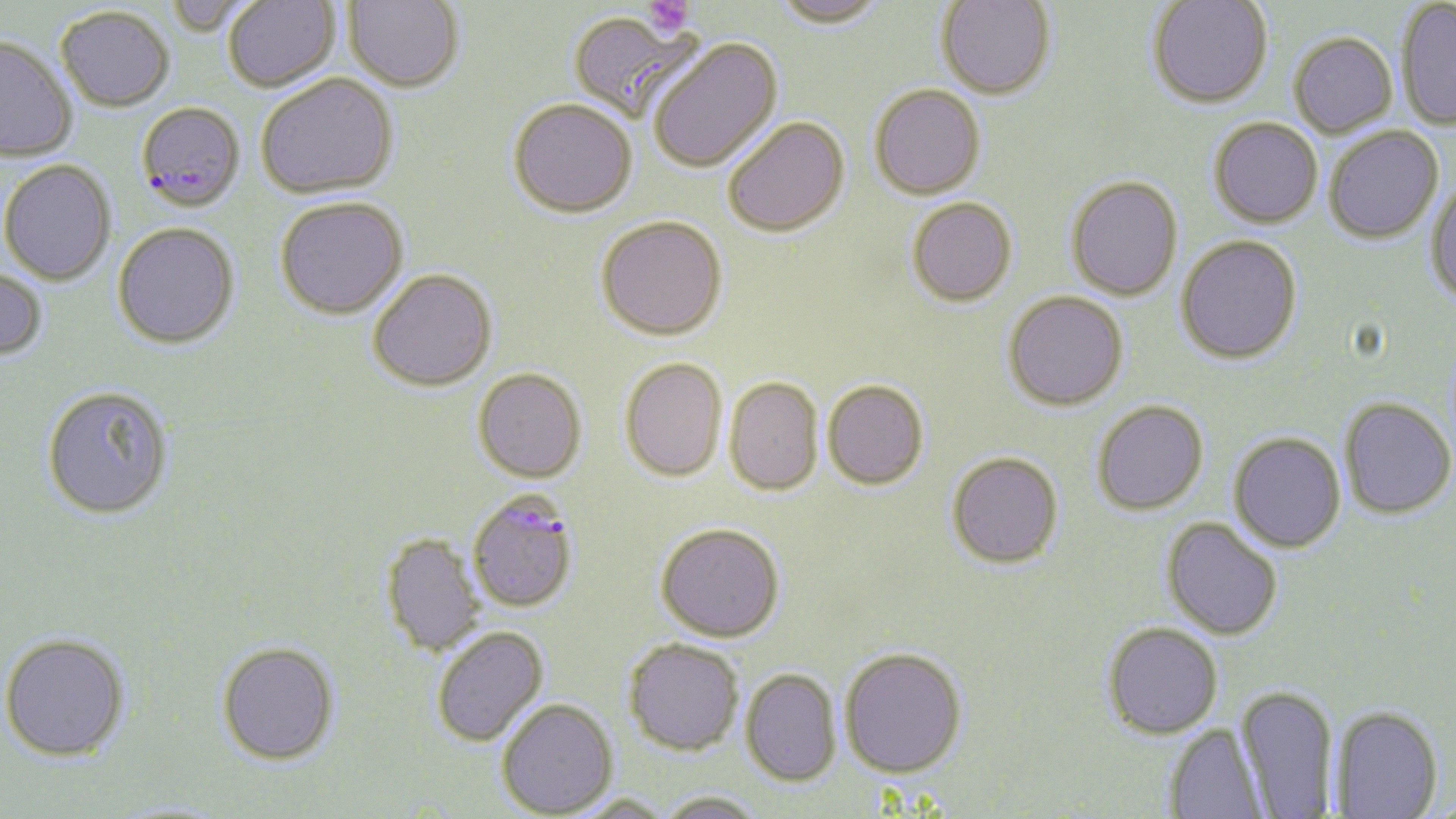

Summary:
  - Coordinate format: approximate bounding boxes as (x1, y1, x2, y2) in pixels
  - Plasmodium falciparum-infected red blood cell locations: (136, 101, 245, 212), (467, 491, 579, 613)
  - Uninfected red blood cell locations: (165, 0, 258, 36), (223, 0, 339, 92), (770, 0, 889, 28), (935, 0, 1056, 99), (1395, 0, 1456, 130), (344, 1, 464, 91), (1147, 1, 1273, 108), (55, 6, 174, 111), (567, 11, 703, 121), (1288, 32, 1397, 137), (0, 35, 78, 162), (646, 38, 783, 173), (255, 73, 398, 198), (869, 83, 986, 199), (509, 97, 637, 217), (723, 116, 849, 236), (1209, 117, 1323, 227), (1324, 125, 1443, 243), (0, 160, 117, 286), (1065, 175, 1183, 301), (1425, 181, 1456, 308), (275, 196, 408, 319), (906, 198, 1017, 306), (596, 214, 727, 340), (113, 222, 239, 349), (1176, 235, 1302, 363), (0, 266, 48, 362), (368, 268, 497, 390), (1003, 290, 1128, 410), (619, 356, 729, 481), (473, 368, 587, 482), (724, 377, 824, 496), (822, 379, 929, 489), (41, 385, 175, 519), (1339, 397, 1455, 519), (1092, 400, 1208, 515), (1229, 431, 1345, 552), (947, 451, 1063, 568), (1162, 517, 1282, 639), (656, 522, 785, 642), (380, 533, 485, 657), (1101, 621, 1223, 739), (430, 626, 548, 747), (1, 632, 131, 762), (623, 637, 744, 756), (216, 641, 340, 764), (839, 646, 968, 777), (740, 668, 841, 786), (1236, 684, 1338, 816), (496, 698, 618, 817), (1333, 705, 1443, 818), (1165, 723, 1269, 819), (655, 791, 765, 819), (565, 794, 678, 819)
  - Platelet locations: (643, 0, 695, 37)
  - Slide-level diagnosis: Plasmodium falciparum
  - Preparation: thin blood smear
  - Stain: May-Grünwald-Giemsa
  - Magnification: 1000x
  - Field of view: single
  - Image size: 1456×819 pixels
  - Modality: optical microscopy